Outline each blood parasite and name the species.
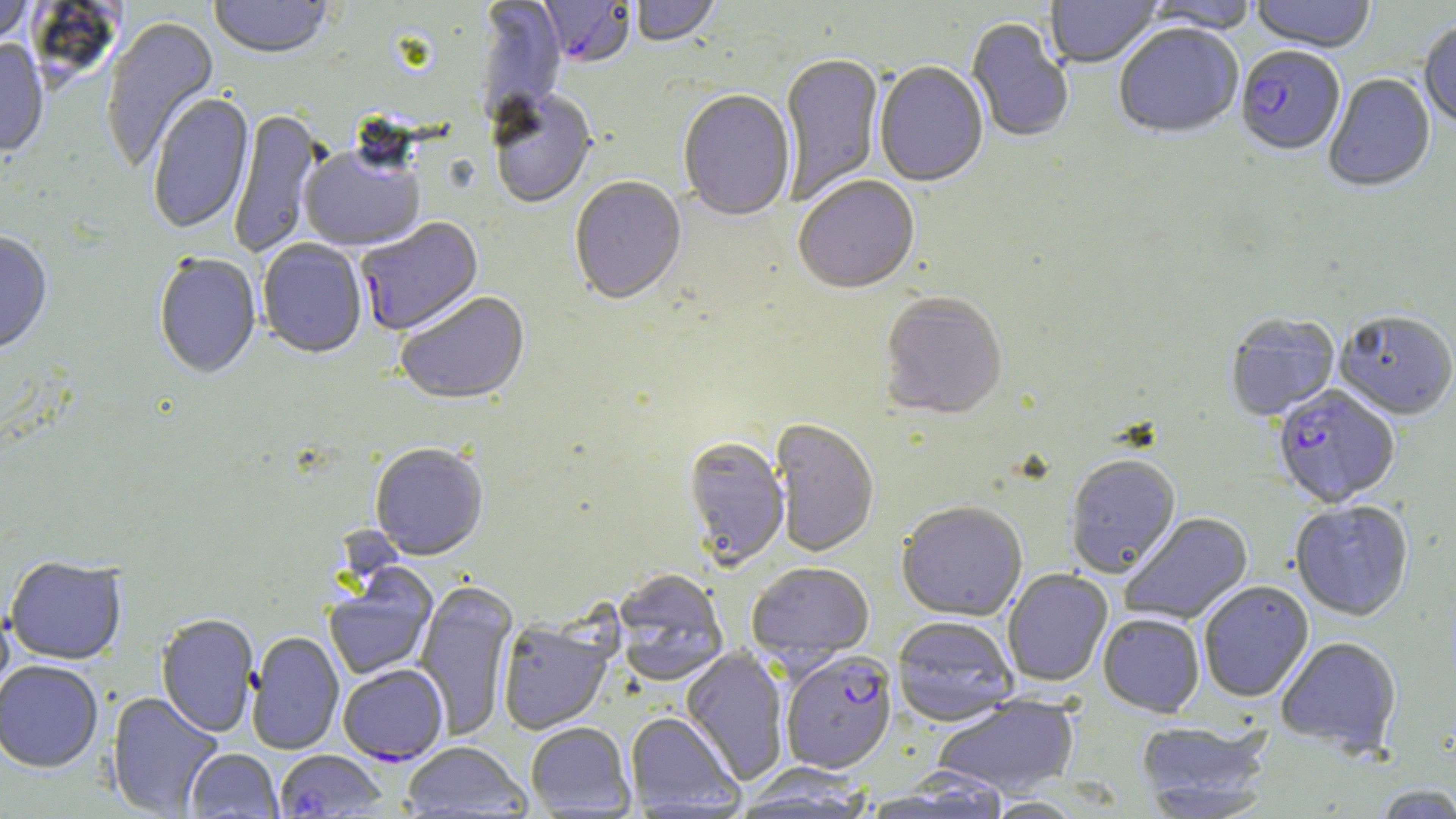
Approximate bounding boxes as (x1, y1, x2, y2) in pixels.
Plasmodium falciparum-infected red blood cells: (536, 0, 636, 71), (1235, 48, 1345, 158), (356, 218, 485, 337), (1274, 386, 1399, 509), (780, 651, 898, 775), (338, 664, 449, 766).
No Plasmodium ovale, Plasmodium malariae, Plasmodium vivax, Babesia divergens, or Trypanosoma brucei observed.

Uninfected red blood cell locations: (209, 0, 332, 61), (631, 0, 722, 50), (1046, 0, 1162, 69), (1143, 0, 1258, 37), (1250, 0, 1376, 55), (0, 1, 35, 51), (475, 1, 565, 125), (101, 17, 221, 173), (967, 19, 1073, 144), (1419, 22, 1456, 128), (1114, 25, 1244, 141), (0, 41, 50, 159), (780, 54, 884, 205), (874, 62, 988, 189), (1323, 74, 1436, 194), (489, 91, 597, 210), (678, 91, 796, 223), (147, 92, 255, 236), (229, 109, 324, 259), (299, 144, 425, 253), (570, 177, 686, 308), (793, 178, 920, 297), (0, 233, 53, 358), (257, 239, 367, 360), (153, 254, 261, 381), (395, 292, 531, 408), (879, 294, 1008, 422), (1335, 313, 1456, 422), (1225, 314, 1340, 422), (770, 419, 879, 558), (683, 438, 789, 570), (370, 444, 489, 562), (1065, 457, 1182, 578), (896, 502, 1028, 623), (1290, 502, 1414, 622), (1120, 512, 1254, 626), (5, 557, 127, 666), (746, 563, 875, 667), (324, 567, 438, 680), (1003, 569, 1113, 687), (614, 570, 729, 686), (414, 580, 518, 741), (1199, 582, 1314, 703), (0, 596, 15, 704), (156, 614, 259, 737), (1098, 615, 1205, 719), (892, 618, 1019, 728), (497, 621, 614, 735), (247, 632, 344, 755), (1276, 638, 1401, 755), (680, 647, 789, 785), (0, 661, 103, 774), (106, 691, 224, 817), (933, 694, 1080, 799), (625, 712, 743, 815), (1136, 720, 1275, 816), (526, 723, 635, 816), (402, 742, 530, 818), (184, 749, 282, 818), (274, 750, 387, 817), (734, 767, 874, 817), (1370, 785, 1456, 818), (983, 797, 1085, 818). Slide-level diagnosis: Plasmodium falciparum. 1000x magnification. Light microscopy. Image is 1456×819 pixels. One field of a larger specimen. May-Grünwald-Giemsa-stained preparation. Thin blood film.